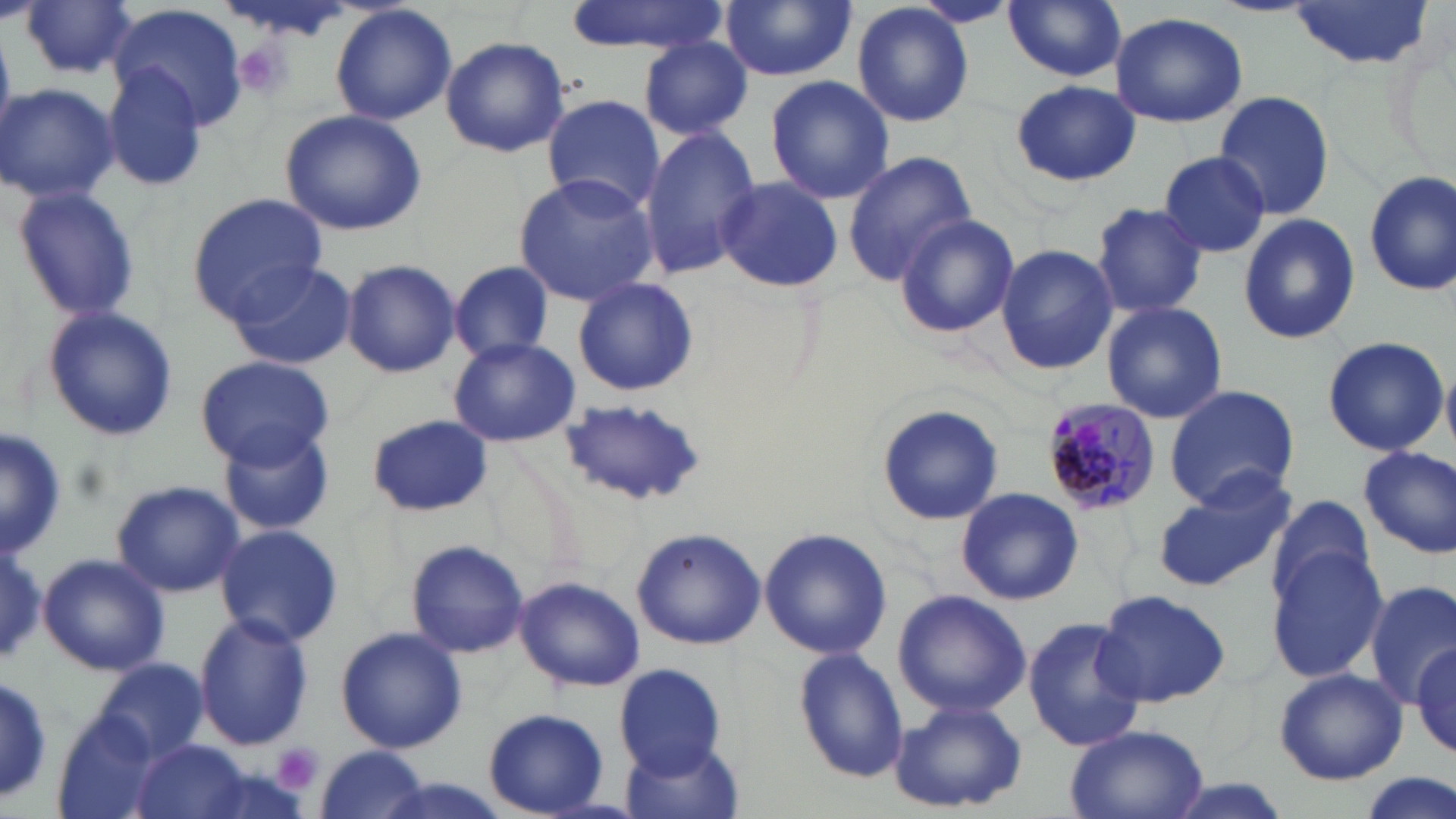
Approximate bounding boxes as (x1,y1)-(x2,y2) corner pairs in pixels. Uninfected red blood cell locations: (562,0)-(733,56), (721,0)-(855,82), (1003,0)-(1127,82), (1210,0)-(1317,17), (1287,0)-(1431,70), (19,1)-(140,81), (909,1)-(1018,29), (329,3)-(457,127), (851,3)-(977,129), (111,4)-(252,134), (1109,12)-(1248,129), (440,34)-(570,157), (639,36)-(753,137), (102,62)-(211,192), (765,75)-(893,204), (1011,80)-(1138,187), (0,83)-(121,206), (1212,90)-(1336,221), (541,95)-(662,214), (278,107)-(428,236), (638,126)-(762,280), (843,150)-(977,282), (1156,150)-(1273,258), (1361,172)-(1455,297), (514,173)-(661,304), (1364,173)-(1456,295), (716,176)-(844,293), (10,185)-(143,321), (186,192)-(327,319), (1092,202)-(1208,317), (892,212)-(1020,338), (1238,212)-(1359,345), (994,244)-(1117,375), (341,258)-(461,377), (227,259)-(358,370), (449,261)-(556,363), (572,278)-(698,396), (1101,301)-(1229,424), (39,306)-(179,442), (1321,335)-(1447,458), (448,338)-(581,447), (192,354)-(335,467), (1162,384)-(1302,513), (556,398)-(707,508), (876,404)-(1004,527), (368,415)-(494,518), (0,426)-(63,562), (221,428)-(335,536), (1359,446)-(1455,558), (1152,476)-(1296,593), (112,479)-(243,598), (956,486)-(1084,606), (1264,494)-(1378,607), (215,523)-(343,647), (760,527)-(892,661), (630,528)-(768,650), (0,537)-(48,670), (404,537)-(529,658), (1266,543)-(1388,683), (37,553)-(171,678), (515,576)-(646,692), (1365,581)-(1456,707), (1094,587)-(1232,708), (892,589)-(1030,719), (193,612)-(315,749), (1023,617)-(1141,752), (334,626)-(469,755), (1412,642)-(1454,755), (792,647)-(910,781), (94,658)-(211,763), (613,663)-(728,775), (1272,668)-(1409,785), (0,675)-(56,801), (888,699)-(1027,814), (483,708)-(610,817), (50,718)-(165,819), (1064,723)-(1208,819), (132,739)-(254,819), (622,739)-(746,819), (313,745)-(429,819), (1351,772)-(1453,819). Plasmodium malariae-infected red blood cell locations: (1037,398)-(1161,512). Platelet locations: (229,37)-(299,100), (273,742)-(322,794). Slide-level diagnosis: Plasmodium malariae. Single field of view. Thin blood smear. Image is 1456×819 pixels. Light microscopy. Captured at 1000x magnification. May-Grünwald-Giemsa-stained preparation.